Locate every blood parasite and identify its species.
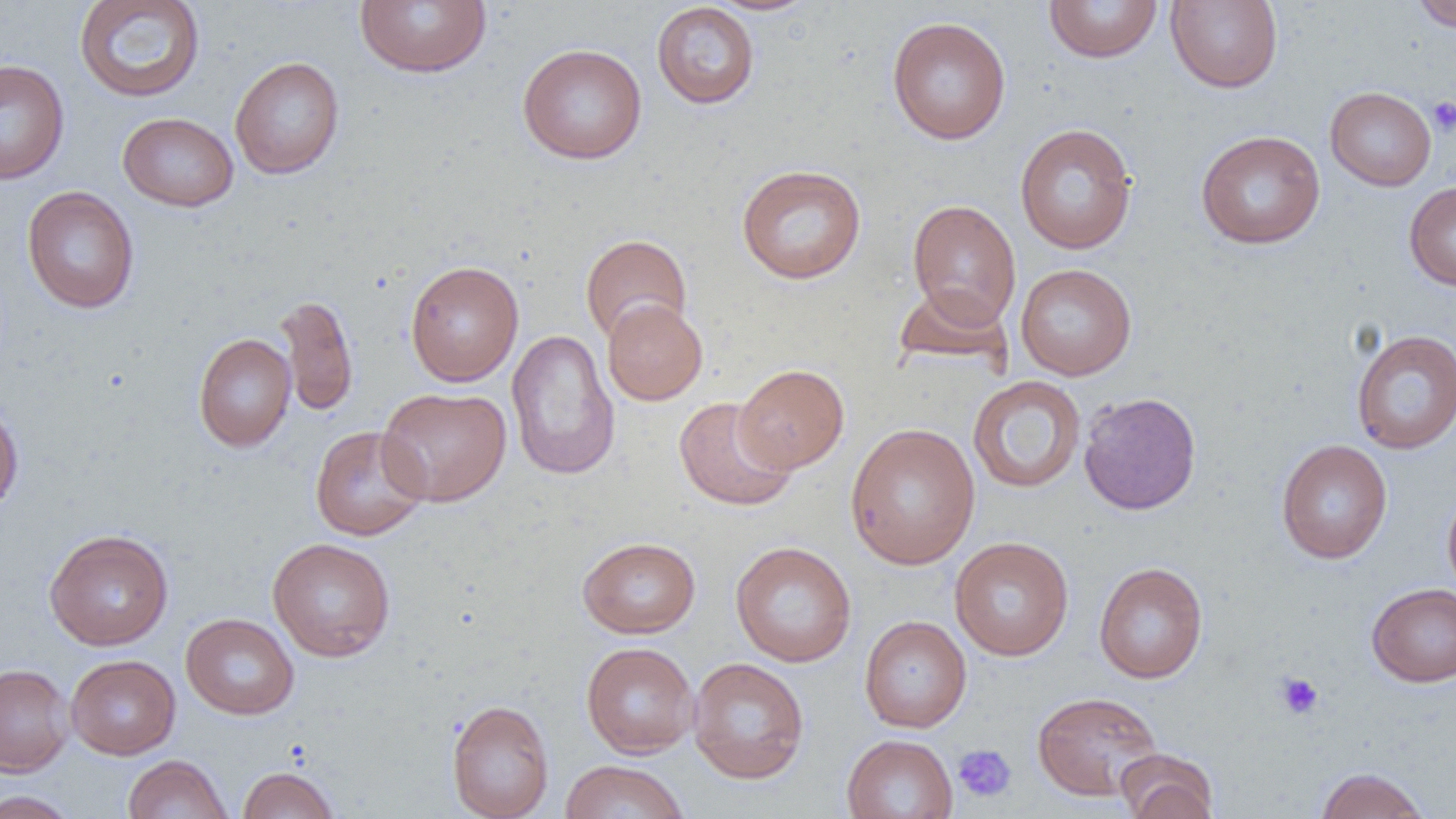

No blood parasites observed.

Summary:
  - Coordinate format: approximate bounding boxes as (x1, y1, x2, y2) in pixels
  - Platelet locations: (1427, 95, 1456, 136), (1275, 672, 1324, 720), (952, 744, 1017, 803)
  - Uninfected red blood cell locations: (74, 0, 206, 103), (706, 0, 823, 16), (1043, 0, 1163, 63), (1165, 0, 1283, 93), (1411, 0, 1456, 32), (355, 1, 491, 78), (651, 2, 759, 109), (886, 16, 1011, 145), (517, 43, 647, 164), (229, 56, 345, 179), (0, 58, 69, 185), (1324, 86, 1437, 191), (117, 112, 238, 211), (1014, 123, 1138, 254), (1195, 130, 1326, 250), (736, 163, 867, 285), (1404, 182, 1456, 291), (22, 185, 139, 314), (906, 199, 1021, 327), (580, 234, 692, 344), (404, 259, 524, 386), (1015, 263, 1137, 380), (892, 284, 1015, 374), (275, 293, 359, 419), (602, 298, 708, 405), (506, 329, 620, 482), (1351, 329, 1456, 454), (193, 333, 296, 452), (734, 364, 849, 473), (968, 376, 1086, 494), (377, 386, 512, 507), (1078, 391, 1202, 515), (673, 396, 797, 511), (0, 401, 24, 516), (845, 422, 981, 570), (309, 425, 430, 541), (1275, 439, 1393, 564), (1442, 488, 1456, 601), (44, 528, 174, 650), (578, 536, 701, 638), (949, 536, 1074, 661), (267, 537, 396, 662), (730, 541, 857, 667), (1093, 561, 1208, 684), (1366, 582, 1456, 687), (180, 612, 299, 720), (859, 615, 972, 732), (581, 641, 699, 758), (66, 654, 180, 759), (687, 657, 810, 784), (0, 663, 74, 776), (1032, 691, 1163, 801), (446, 698, 555, 819), (842, 733, 958, 819), (1116, 749, 1219, 819), (123, 754, 233, 819), (560, 760, 691, 819), (237, 766, 340, 819), (1314, 766, 1432, 819), (0, 790, 81, 818)
  - Slide-level diagnosis: negative for blood parasites
  - Modality: optical microscopy
  - Magnification: 1000x
  - Field of view: one of a larger specimen
  - Preparation: thin blood film
  - Image size: 1456×819 pixels